Comment on the morphology of the erythrocytes.
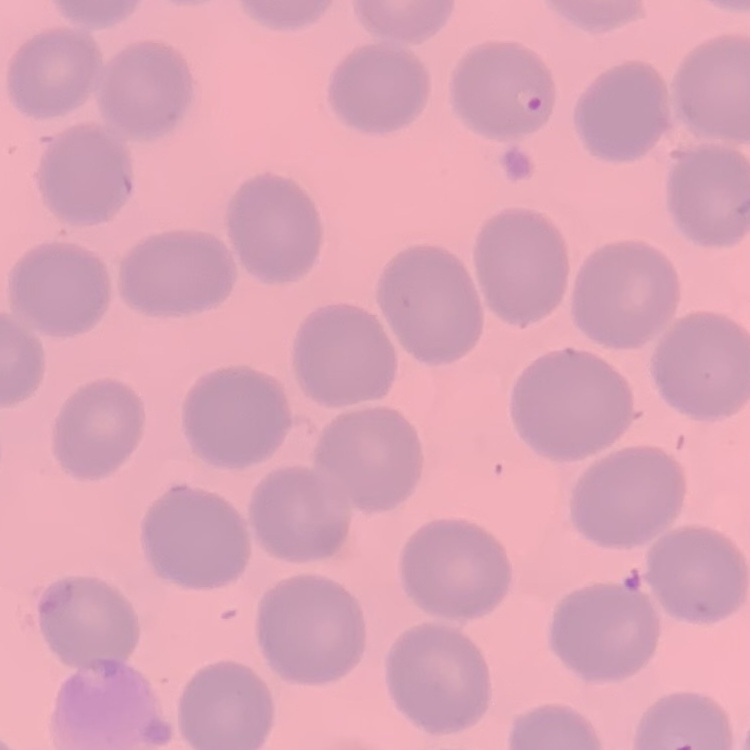
They show no rouleaux formation.

Summary:
  - Stain: Field's or Giemsa
  - Preparation: thin blood film
  - Image type: one tile cut from a larger photomicrograph